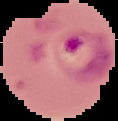
Summary:
  - Malaria status: parasitized
  - Image type: cell region segmented out of the field of view; surrounding area masked to black
  - Image size: 118×121 pixels
  - Preparation: thin blood film